Assess the morphology of the red blood cells.
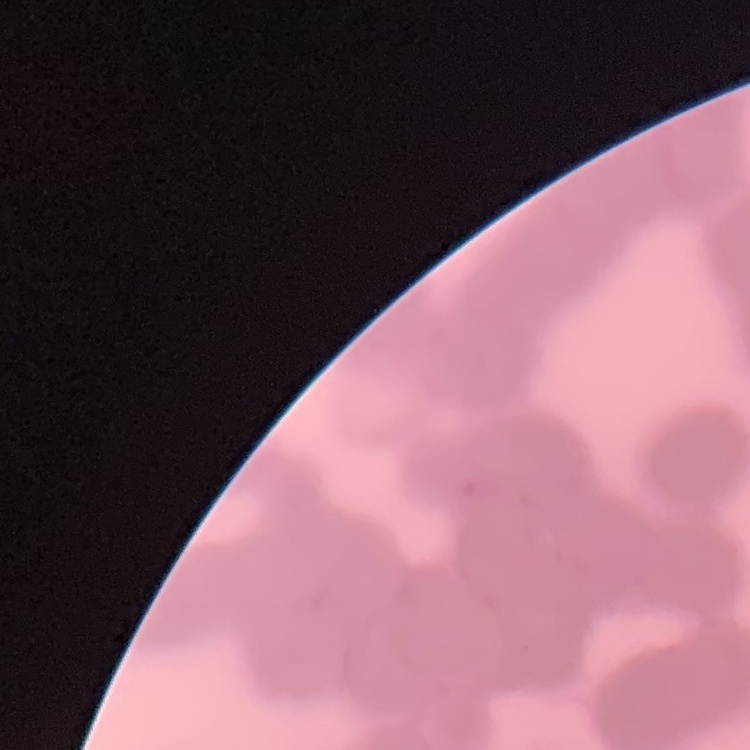

They show rouleaux formation.

Summary:
  - Preparation: thin blood film
  - Stain: Field's or Giemsa
  - Image type: one tile cut from a larger photomicrograph